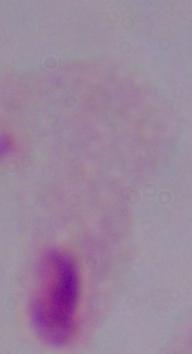
Summary:
  - Modality: micrograph
  - Magnification: 1000x
  - Identification: trichomonad